Report the malaria status of this cell.
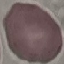

It is uninfected.

capture = smartphone through the microscope eyepiece
preparation = thin blood film
image type = automatically extracted cell patch, resized to 64 × 64 pixels
stain = Giemsa